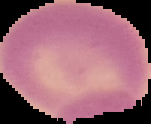 Image is 151×124 pixels. From a thin blood film. Result: negative for Plasmodium parasites. The area outside the segmented cell region is set to black.